Classify this cell by malaria status.
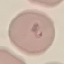

It is parasitized.

Summary:
  - Preparation: thin blood film
  - Capture: smartphone camera at the microscope eyepiece
  - Stain: Giemsa
  - Image type: cell patch, automatically extracted from a larger field of view and resized to 64 × 64 pixels